Locate every P. falciparum parasite and give its life-cycle stage, and locate every leukocyte and any debris.
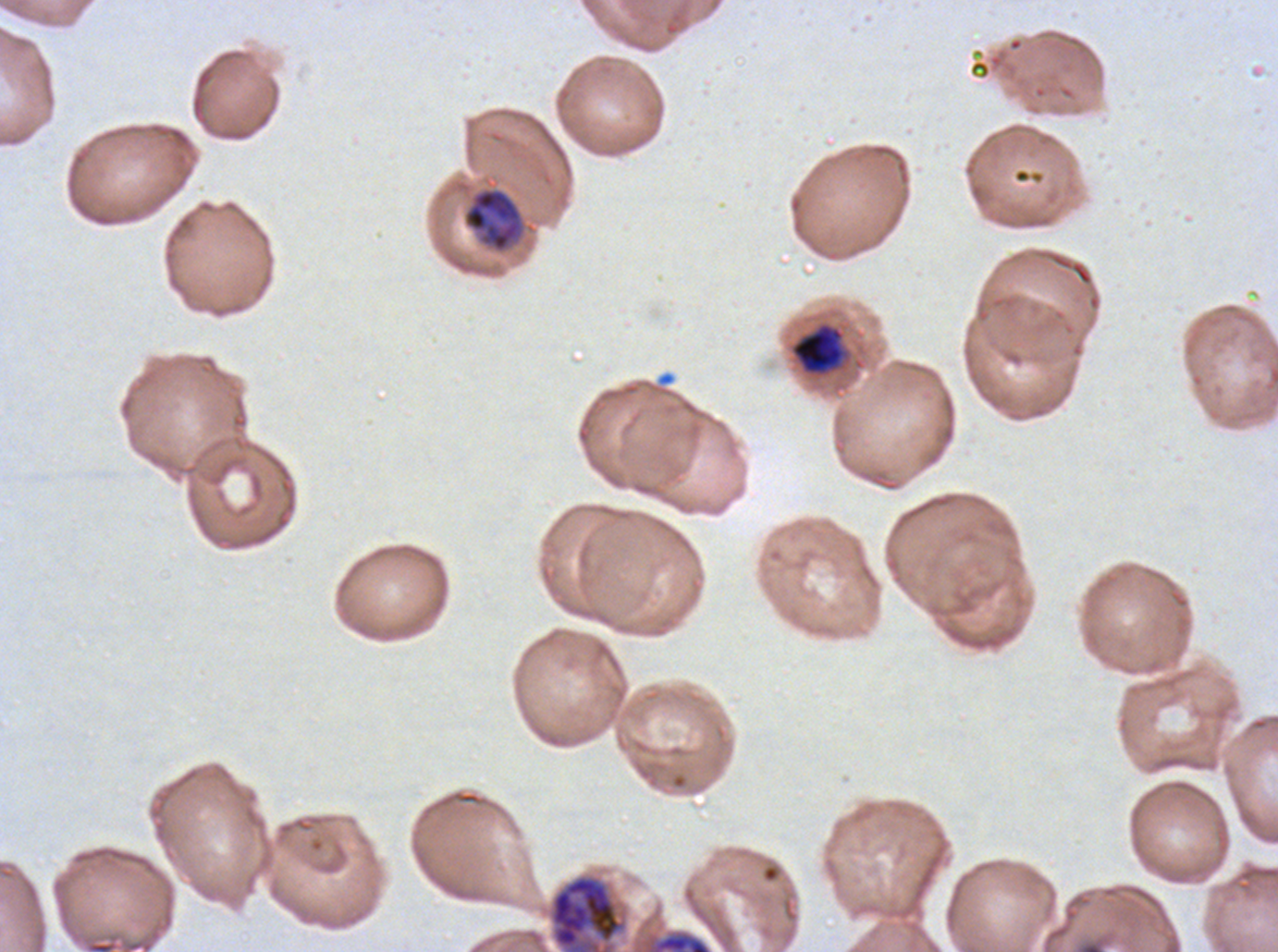

Approximate bounding boxes as (x1, y1, x2, y2) in pixels.
Mid trophozoites: (463, 188, 523, 252), (791, 323, 844, 374).
Late trophozoites: (650, 931, 712, 951).
Late schizonts: (548, 874, 627, 951).
No rings, late-ring/early-trophozoite forms, early schizonts, segmenters, gametocytes, leukocytes, or debris observed.

field_of_view: sub-image separated from a larger composite
life_cycle_stages_observed: mid trophozoite, late trophozoite, late schizont
image_size: 1278×952 pixels
specimen: P. falciparum from a patient in The Gambia, cultured ex vivo for 24 to 48 hours
stain: Giemsa
preparation: thin blood film